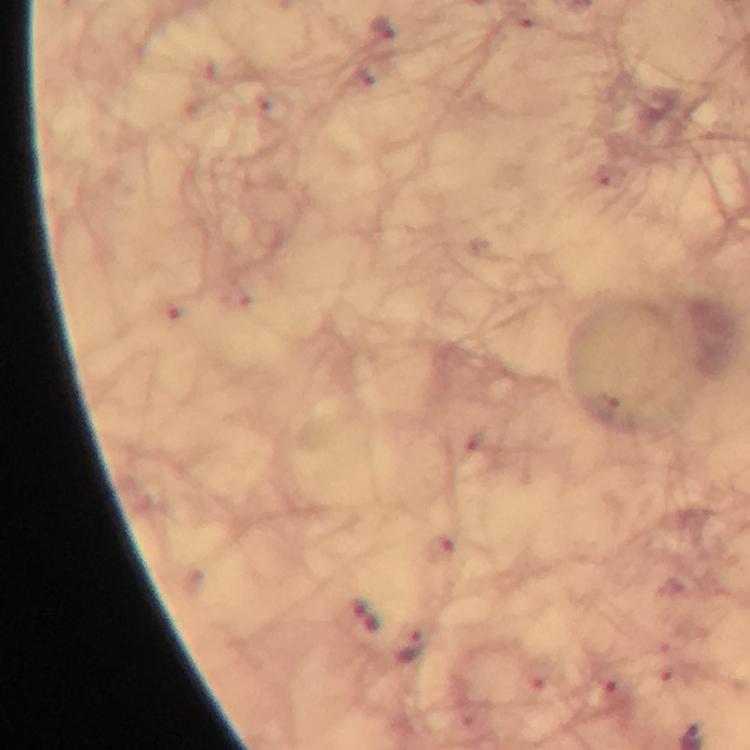

image size = 750×750 pixels
cropped from = one field of view
stain = Giemsa
magnification = 100x
immersion oil = applied
Plasmodium parasite locations = approximate centers as (x, y) in pixels: (363, 616), (407, 645)
preparation = thick smear
context = from a malaria diagnostic workup
capture = smartphone camera through the microscope